Outline each blood parasite and name the species.
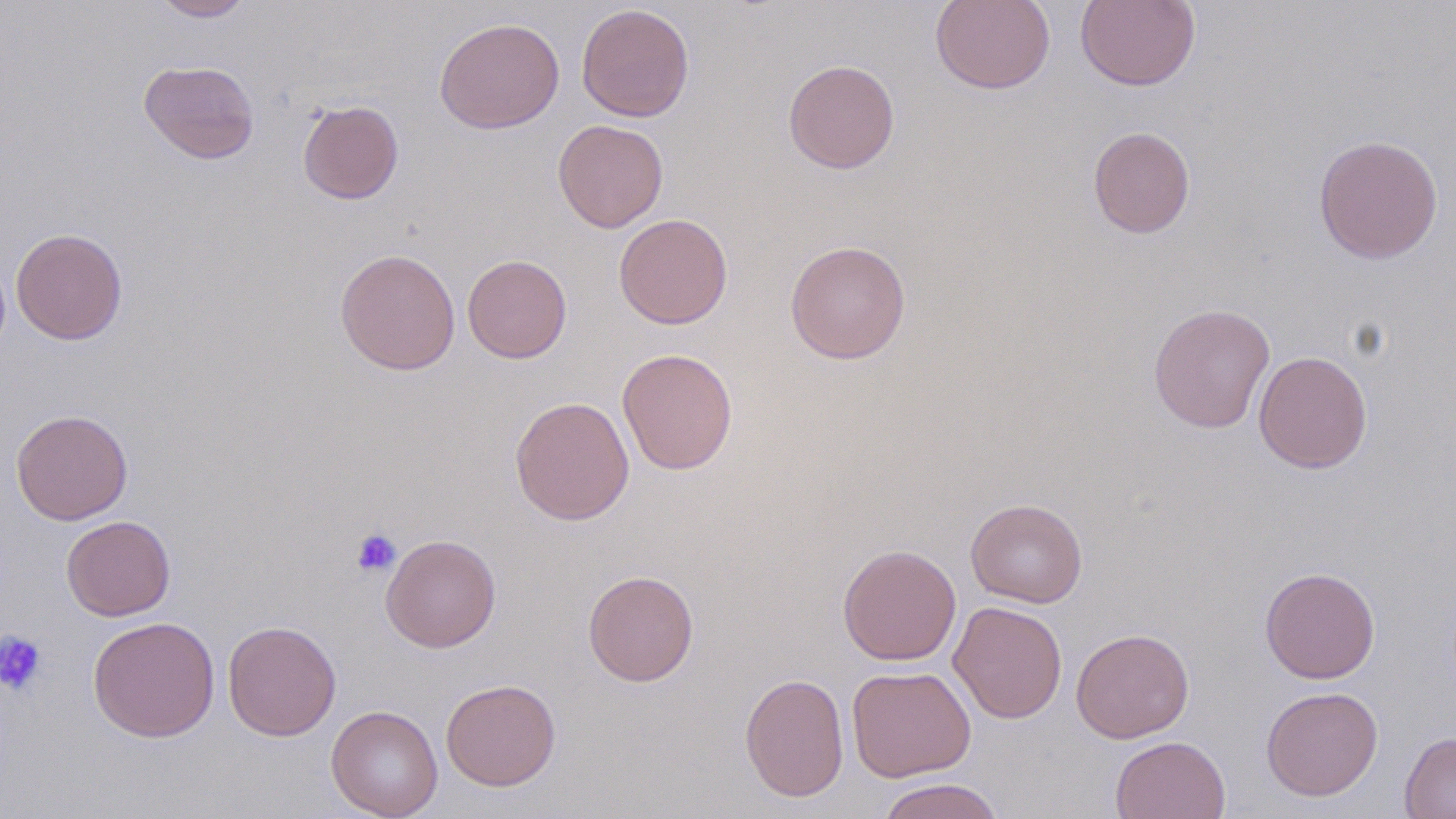

No blood parasites observed.

slide-level diagnosis = no evidence of blood parasites
stain = May-Grünwald-Giemsa
field of view = single
preparation = thin blood film
image size = 1456×819 pixels
magnification = 1000x
platelet locations = approximate bounding boxes as [x1, y1, x2, y2] in pixels: [351, 528, 401, 577], [0, 630, 48, 696]
modality = light microscopy
uninfected red blood cell locations = approximate bounding boxes as [x1, y1, x2, y2] in pixels: [151, 0, 257, 21], [930, 0, 1055, 95], [1075, 0, 1200, 91], [576, 4, 694, 122], [434, 16, 564, 134], [783, 59, 900, 174], [139, 60, 260, 164], [297, 100, 404, 204], [552, 119, 669, 233], [1087, 126, 1195, 238], [1313, 134, 1443, 264], [613, 213, 733, 329], [11, 228, 128, 345], [785, 240, 911, 364], [334, 248, 461, 375], [462, 254, 573, 363], [1148, 303, 1275, 433], [617, 348, 738, 475], [1253, 350, 1373, 474], [509, 395, 635, 525], [11, 409, 133, 525], [966, 498, 1087, 607], [61, 515, 176, 621], [381, 534, 501, 652], [837, 543, 962, 665], [1259, 567, 1380, 684], [583, 569, 699, 686], [949, 601, 1068, 724], [87, 615, 220, 742], [222, 619, 341, 741], [1071, 628, 1194, 743], [847, 665, 976, 782], [739, 672, 849, 802], [440, 678, 562, 791], [1261, 686, 1384, 801], [326, 704, 443, 819], [1399, 731, 1456, 818], [1110, 735, 1230, 819], [874, 778, 1007, 819]